Assess this cell for malaria.
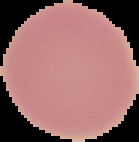

Uninfected.

Cell region segmented out of the field of view; the surrounding area is masked to black. From a thin blood film. Image is 139×142 pixels.